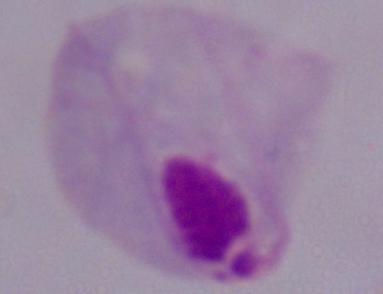
Captured at 1000x magnification. A trichomonad is shown. Micrograph.